State which cell type is depicted.
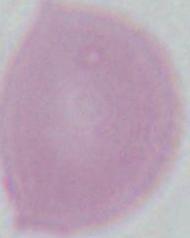
This is an erythrocyte.

{
  "modality": "micrograph",
  "magnification": "1000x"
}